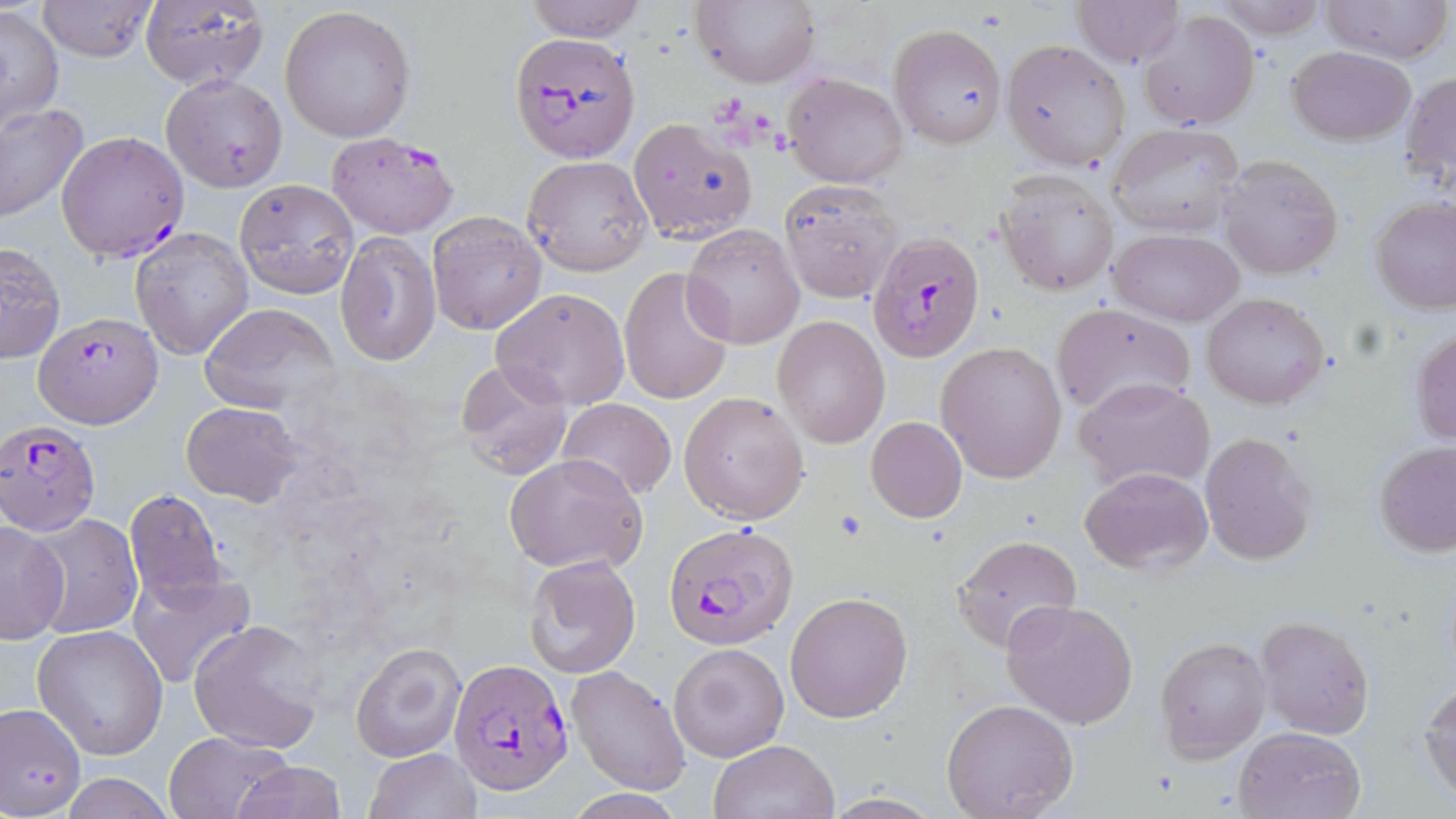

Summary:
  - Coordinate format: approximate bounding boxes as (x1,y1)-(x2,y2) corner pairs in pixels
  - Plasmodium falciparum-infected red blood cell locations: (509,34)-(638,161), (57,130)-(189,262), (326,131)-(460,239), (868,231)-(986,364), (33,311)-(164,427), (0,420)-(98,535), (664,519)-(799,651), (449,658)-(575,796)
  - Uninfected red blood cell locations: (36,0)-(159,61), (523,0)-(649,42), (692,0)-(819,88), (1073,0)-(1184,66), (1207,0)-(1328,39), (1318,0)-(1452,65), (139,1)-(271,91), (280,4)-(418,142), (2,6)-(65,129), (1137,9)-(1259,130), (889,24)-(1006,148), (1002,39)-(1131,169), (1286,45)-(1415,145), (1402,70)-(1456,191), (782,71)-(909,188), (161,73)-(286,192), (0,102)-(89,223), (627,117)-(759,244), (1108,123)-(1246,240), (1216,154)-(1343,279), (523,155)-(652,275), (996,171)-(1119,296), (234,179)-(360,299), (778,179)-(902,303), (1371,196)-(1456,313), (425,209)-(547,335), (682,224)-(805,348), (130,226)-(253,359), (1109,228)-(1243,327), (336,230)-(441,369), (0,241)-(65,364), (618,266)-(735,406), (491,287)-(631,411), (1200,292)-(1329,409), (1051,301)-(1197,419), (198,304)-(340,413), (772,315)-(890,448), (1409,325)-(1456,447), (937,342)-(1066,483), (455,359)-(574,481), (1075,377)-(1214,493), (681,391)-(809,523), (557,398)-(675,501), (182,401)-(301,505), (866,417)-(967,522), (1199,433)-(1317,566), (1374,440)-(1456,559), (504,452)-(647,573), (1080,465)-(1212,573), (123,489)-(228,605), (28,513)-(142,639), (0,521)-(69,643), (950,533)-(1082,653), (523,554)-(640,679), (128,567)-(255,689), (784,591)-(912,724), (1001,599)-(1137,729), (1255,614)-(1375,740), (190,619)-(326,752), (33,624)-(169,759), (1156,636)-(1269,760), (350,641)-(467,764), (669,641)-(789,762), (565,665)-(690,794), (1420,679)-(1456,801), (939,699)-(1079,818), (0,701)-(87,816), (1233,726)-(1366,819), (163,731)-(292,818), (708,739)-(839,819), (365,748)-(480,819), (231,761)-(348,818), (60,774)-(177,817), (818,792)-(947,818)
  - Slide-level diagnosis: Plasmodium falciparum
  - Preparation: thin blood film
  - Field of view: single
  - Image size: 1456×819 pixels
  - Magnification: 1000x
  - Stain: May-Grünwald-Giemsa
  - Modality: light microscopy